Describe the morphology of the red blood cells.
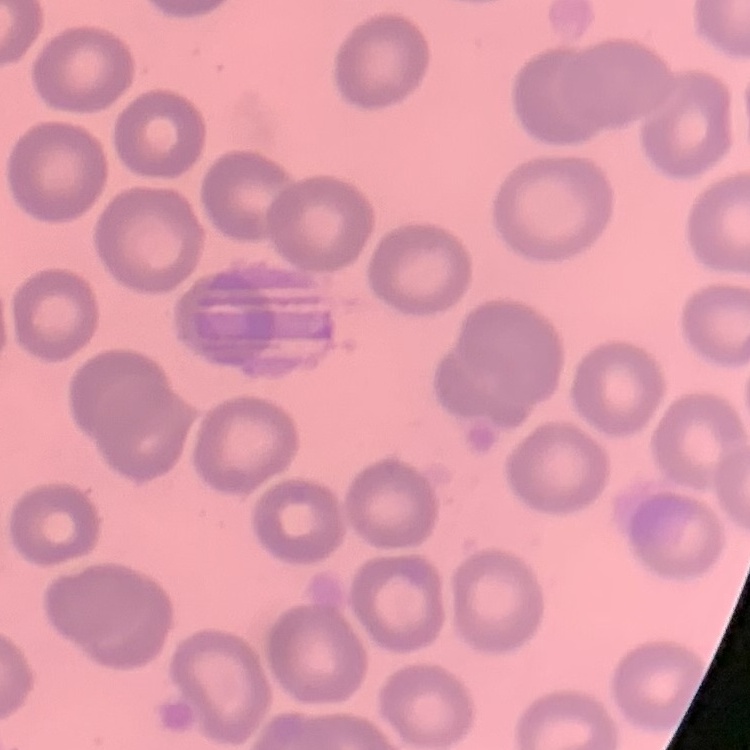
They show no rouleaux formation.

Square crop of a larger photomicrograph. Thin blood film. Field's or Giemsa stain.